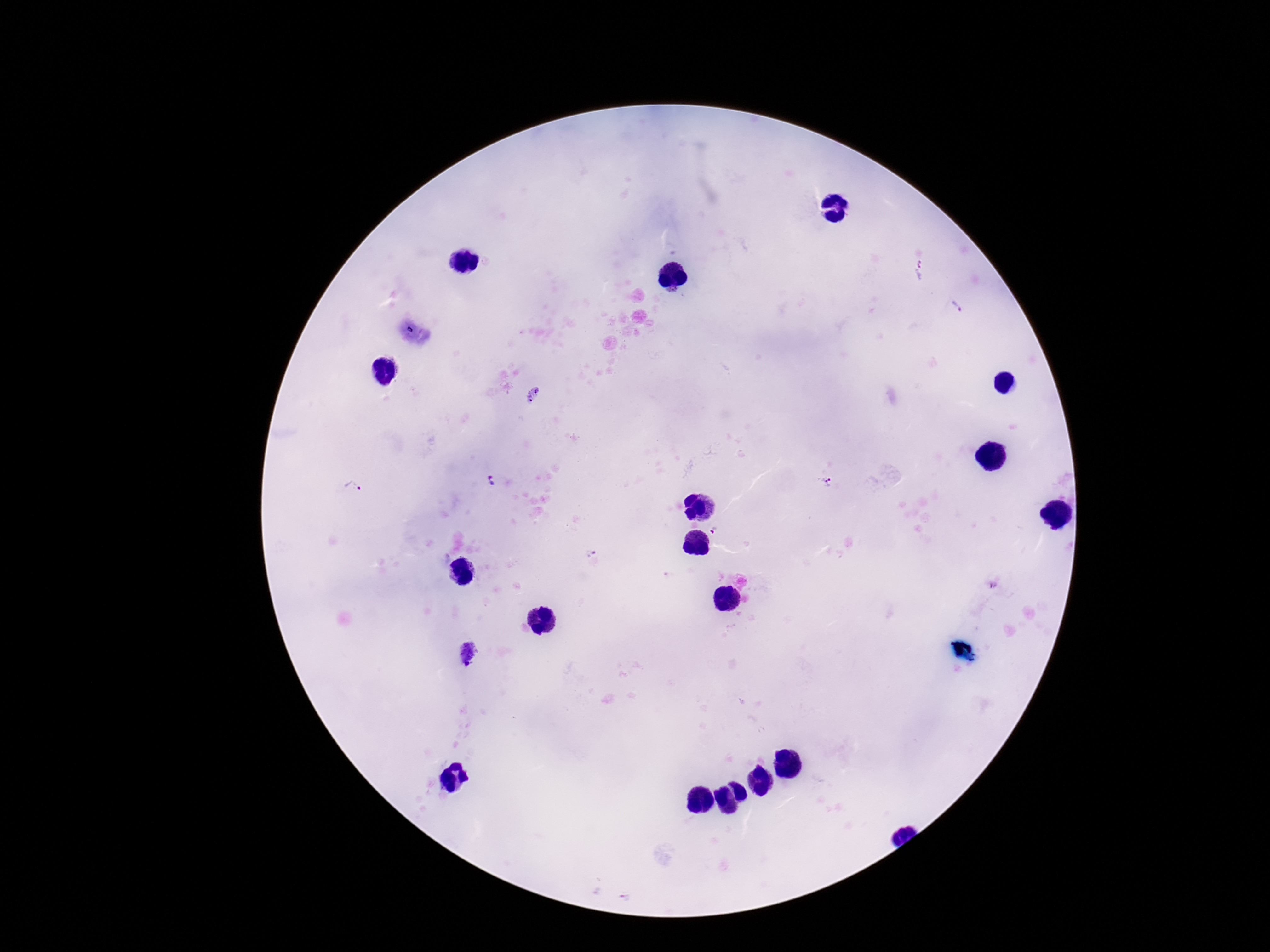

capture = smartphone camera through the microscope eyepiece
stain = Giemsa
magnification = 100x
preparation = thick peripheral-blood smear
image size = 1270×952 pixels
field of view = single
Plasmodium parasite locations = approximate centers as (x, y) in pixels: (922, 271), (957, 307), (534, 395), (489, 477), (827, 482), (492, 483), (352, 488), (716, 530), (993, 585), (468, 653), (625, 897)
patient malaria status = positive